Classify this cell by malaria status.
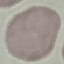
Uninfected.

Automatically extracted cell patch, resized to 64 × 64 pixels. Acquired by smartphone through the microscope eyepiece. Giemsa-stained preparation. Thin blood smear.